Describe the morphology of the red blood cells.
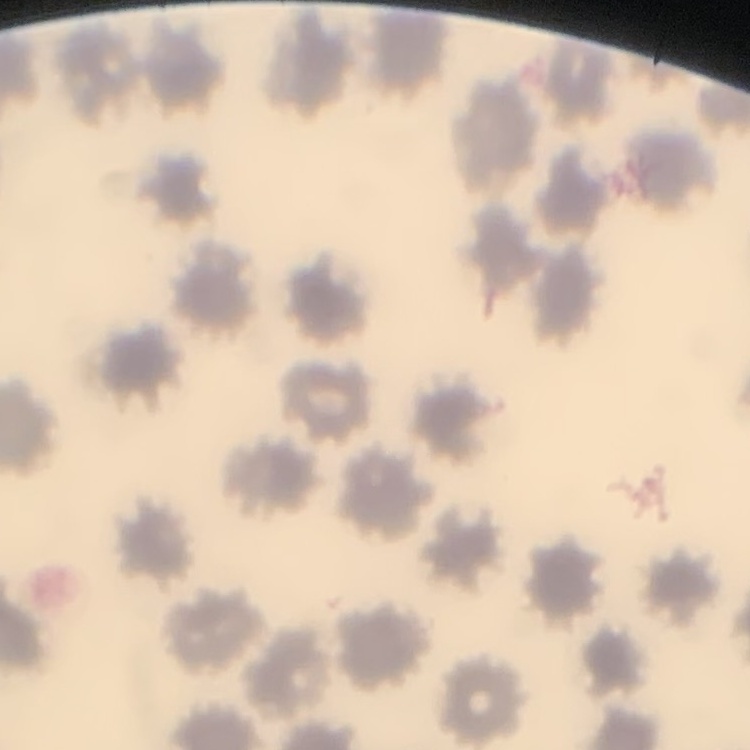
They show no rouleaux formation.

Thin blood film. Stained with either Field's or Giemsa. One tile cut from a larger photomicrograph.